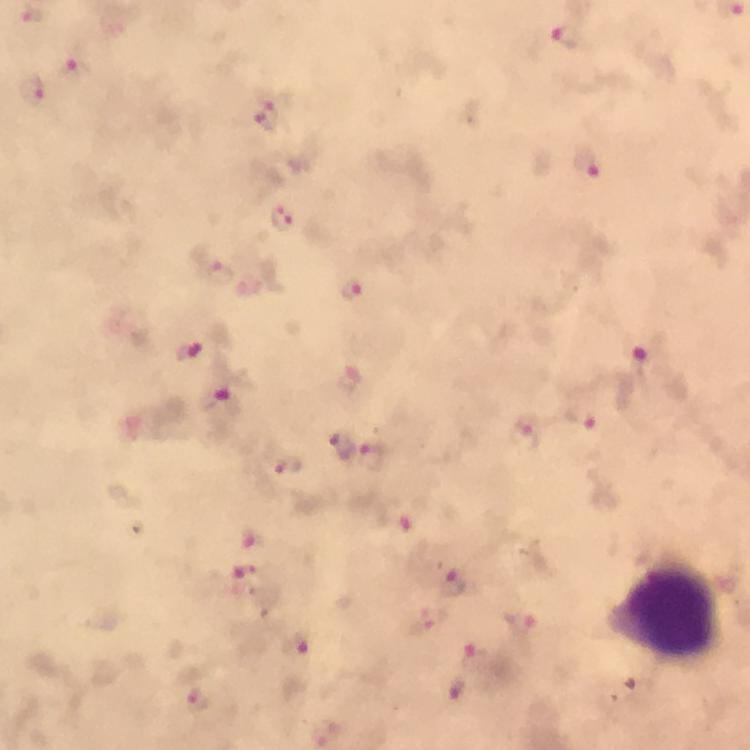

Approximate object centers, in pixels from the top-left corner.
Summary:
  - Plasmodium parasite locations: (x=567, y=35), (x=73, y=68), (x=31, y=88), (x=268, y=117), (x=587, y=163), (x=282, y=218), (x=219, y=271), (x=351, y=288), (x=189, y=353), (x=639, y=364), (x=216, y=399), (x=343, y=445), (x=373, y=456), (x=287, y=464), (x=394, y=522), (x=253, y=537), (x=245, y=572), (x=453, y=583), (x=428, y=619), (x=519, y=620), (x=294, y=642), (x=475, y=658), (x=459, y=687), (x=198, y=698)
  - Leukocyte locations: (x=667, y=606)
  - Preparation: thick smear
  - Magnification: 100x
  - Stain: Giemsa
  - Cropped from: a single field of view
  - Immersion oil: applied
  - Context: from a diagnostic examination for malaria
  - Image size: 750×750 pixels
  - Capture: smartphone mounted on the microscope